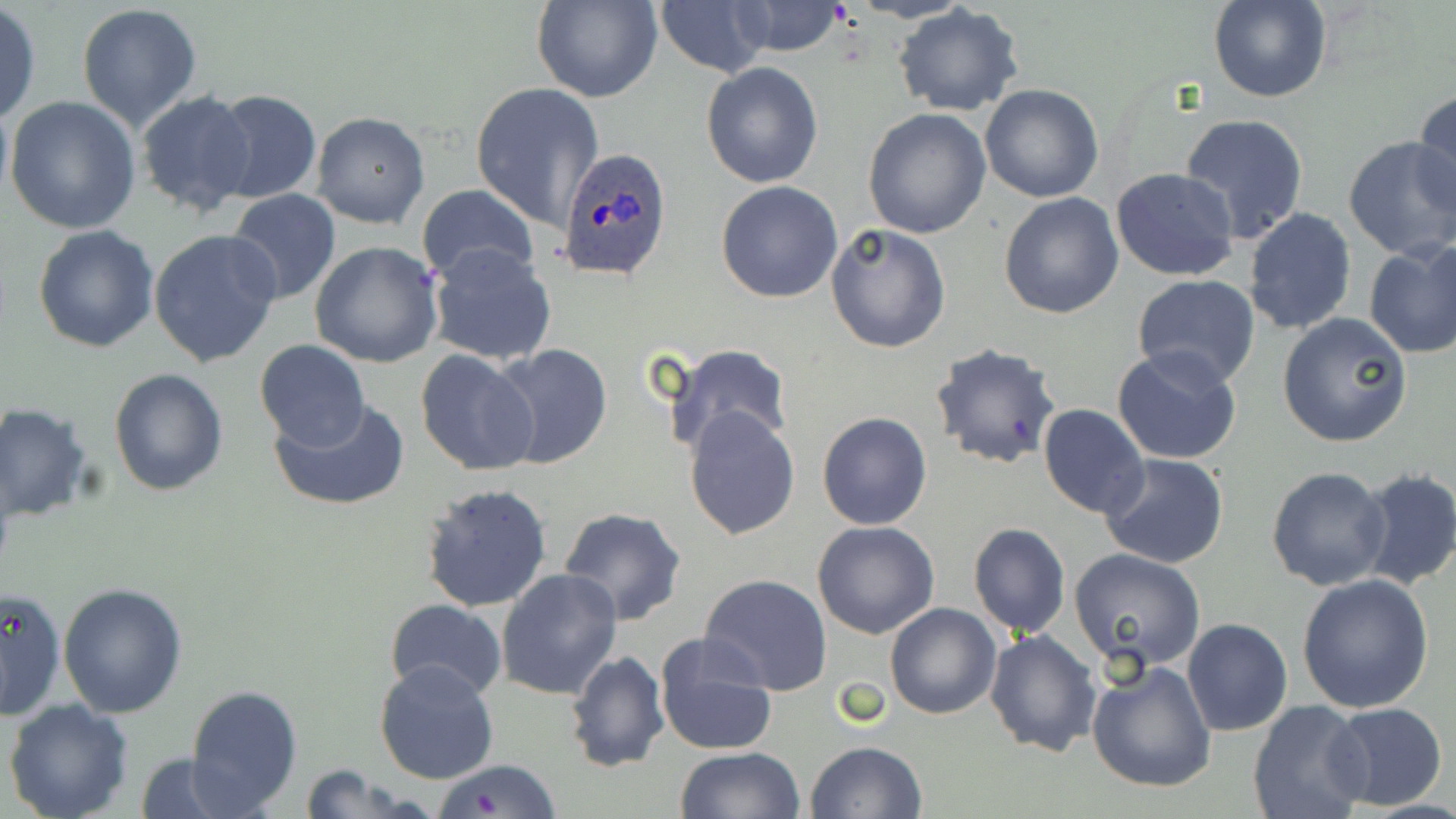
slide-level diagnosis = Plasmodium ovale
field of view = single
Plasmodium ovale-infected red blood cell locations = approximate bounding boxes as (x1,y1)-(x2,y2) corner pairs in pixels: (556,144)-(674,282)
image size = 1456×819 pixels
preparation = thin blood smear
modality = optical microscopy
magnification = 1000x
uninfected red blood cell locations = approximate bounding boxes as (x1,y1)-(x2,y2) corner pairs in pixels: (534,0)-(661,103), (1207,0)-(1331,103), (652,2)-(767,76), (721,2)-(851,57), (894,4)-(1024,116), (76,5)-(203,132), (0,6)-(41,124), (701,62)-(824,188), (470,81)-(604,231), (980,84)-(1105,202), (1411,88)-(1456,222), (209,89)-(321,205), (134,90)-(259,217), (5,95)-(141,233), (863,109)-(991,239), (311,111)-(430,229), (1180,113)-(1310,243), (1342,136)-(1456,262), (1111,166)-(1239,281), (716,180)-(843,302), (418,184)-(539,291), (227,190)-(342,307), (999,192)-(1123,319), (1243,207)-(1357,334), (826,223)-(949,354), (33,224)-(160,353), (149,228)-(282,369), (310,241)-(443,368), (1363,241)-(1456,358), (427,244)-(557,366), (1131,274)-(1261,389), (1277,312)-(1413,448), (254,338)-(369,450), (660,343)-(794,460), (930,343)-(1061,469), (488,344)-(613,469), (1112,347)-(1242,464), (414,349)-(540,478), (109,367)-(228,498), (270,398)-(410,512), (0,402)-(94,522), (1038,403)-(1149,519), (683,405)-(800,540), (818,412)-(932,530), (1098,453)-(1229,570), (1267,466)-(1392,590), (1353,467)-(1456,591), (420,482)-(552,612), (557,506)-(689,627), (812,521)-(941,640), (968,522)-(1070,639), (1068,549)-(1207,675), (495,568)-(622,700), (698,573)-(833,696), (1297,573)-(1434,713), (59,583)-(189,718), (0,586)-(65,719), (385,600)-(509,701), (884,601)-(1001,719), (1182,618)-(1291,737), (984,629)-(1101,757), (651,633)-(779,756), (563,648)-(669,773), (1086,659)-(1218,793), (373,660)-(500,785), (184,683)-(302,814), (4,699)-(135,819), (1247,701)-(1372,819), (1323,702)-(1448,811), (806,741)-(927,819), (675,747)-(803,819), (132,753)-(246,819), (432,759)-(562,818), (293,765)-(425,819)
stain = May-Grünwald-Giemsa